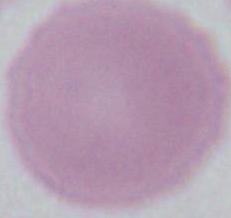
magnification = 1000x
identification = erythrocyte
modality = micrograph